Assess this cell for malaria.
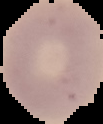

It is uninfected.

Image is 103×124 pixels. From a thin blood smear. Segmented cell region on a black background.